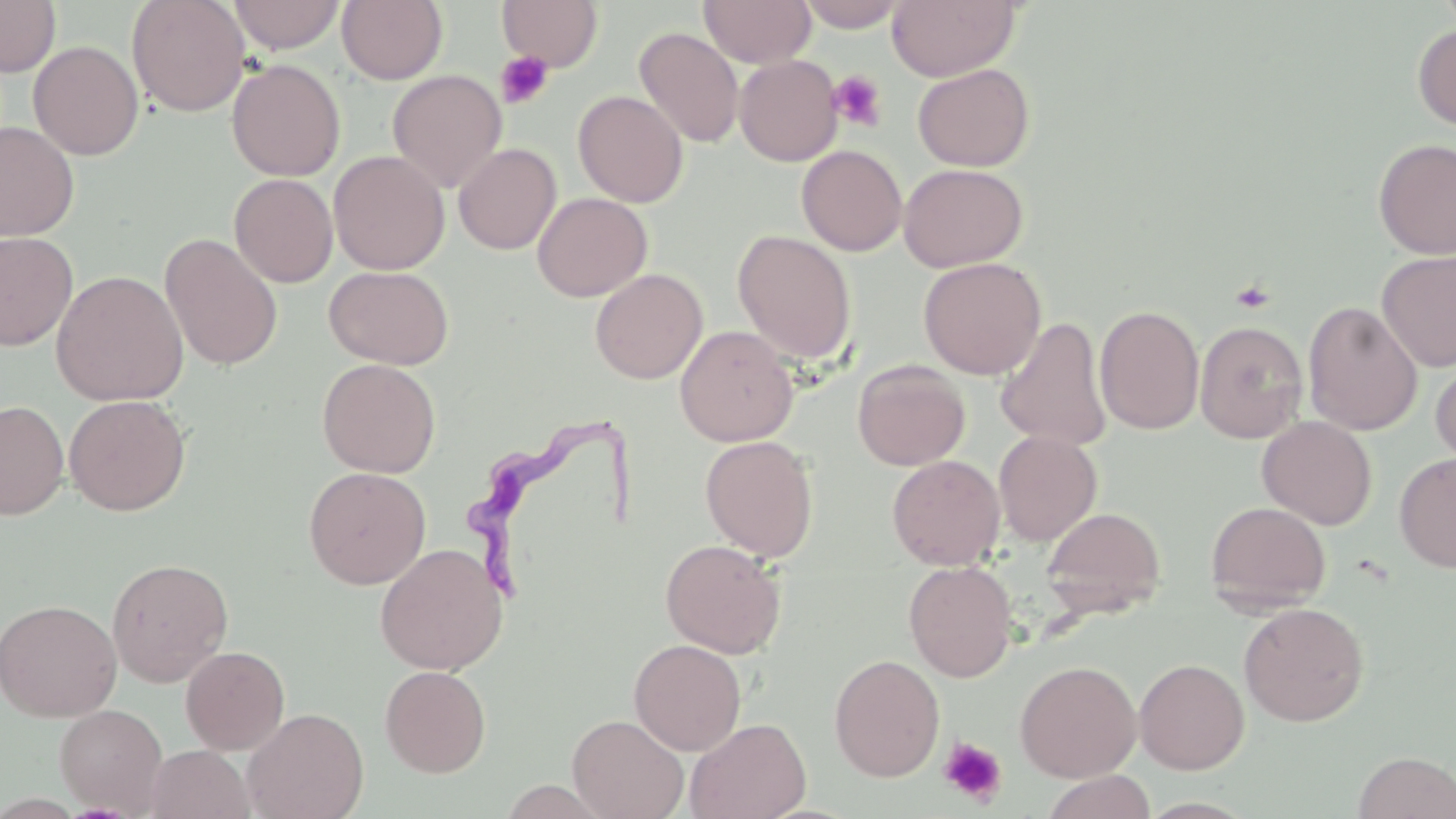

Summary:
  - Coordinate format: approximate bounding boxes as (x1, y1, x2, y2) in pixels
  - Uninfected red blood cell locations: (0, 0, 61, 76), (126, 0, 250, 117), (228, 0, 345, 54), (337, 0, 448, 85), (698, 0, 817, 68), (796, 0, 909, 32), (887, 0, 1020, 82), (497, 1, 604, 71), (1412, 24, 1456, 131), (634, 26, 744, 149), (28, 41, 144, 160), (734, 55, 843, 166), (227, 59, 345, 181), (912, 63, 1035, 171), (387, 69, 508, 193), (573, 90, 688, 207), (0, 121, 79, 241), (1373, 138, 1456, 259), (453, 143, 561, 255), (796, 145, 907, 256), (328, 150, 450, 275), (898, 162, 1028, 272), (229, 173, 338, 287), (532, 191, 652, 301), (733, 230, 857, 366), (0, 231, 78, 351), (160, 233, 283, 371), (1376, 250, 1456, 373), (918, 257, 1047, 379), (324, 265, 454, 369), (590, 268, 708, 383), (51, 269, 189, 407), (1302, 301, 1422, 436), (1095, 304, 1205, 435), (994, 317, 1112, 452), (1196, 320, 1308, 443), (674, 325, 799, 446), (317, 358, 440, 478), (852, 359, 971, 471), (1431, 359, 1456, 472), (64, 394, 190, 516), (0, 400, 69, 520), (1257, 416, 1377, 529), (993, 430, 1102, 545), (700, 435, 819, 562), (1394, 453, 1456, 573), (887, 454, 1005, 570), (303, 466, 431, 589), (1205, 501, 1331, 611), (1041, 506, 1166, 619), (660, 538, 787, 658), (374, 542, 507, 675), (106, 557, 234, 687), (904, 561, 1017, 682), (0, 598, 122, 722), (1239, 602, 1370, 726), (629, 638, 746, 755), (180, 645, 290, 754), (829, 654, 945, 782), (1134, 658, 1250, 774), (1014, 660, 1142, 782), (380, 665, 492, 777), (54, 704, 168, 815), (242, 707, 369, 819), (567, 713, 688, 819), (685, 717, 811, 819), (145, 745, 254, 819), (1353, 751, 1456, 818), (1040, 770, 1156, 819)
  - Trypanosoma brucei locations: (469, 411, 634, 608)
  - Platelet locations: (495, 50, 555, 109), (828, 70, 888, 132), (1230, 279, 1275, 313), (939, 737, 1007, 806)
  - Slide-level diagnosis: Trypanosoma brucei
  - Image size: 1456×819 pixels
  - Magnification: 1000x
  - Stain: May-Grünwald-Giemsa
  - Modality: light microscopy
  - Preparation: thin blood film
  - Field of view: one of a larger specimen